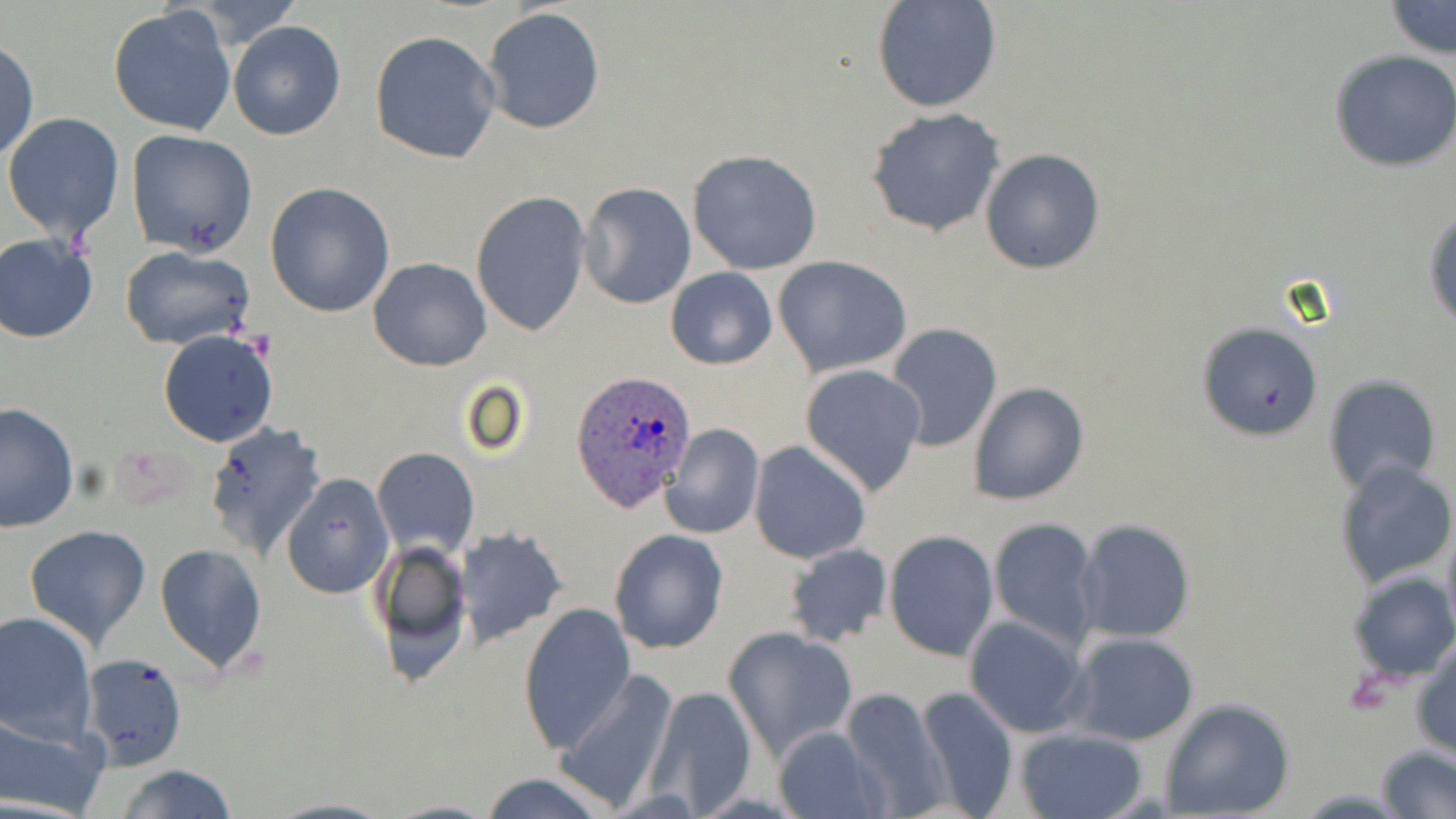 Approximate bounding boxes as [x1, y1, x2, y2] in pixels. Uninfected red blood cell locations: [192, 0, 300, 47], [871, 0, 1001, 114], [1385, 2, 1454, 59], [108, 5, 237, 135], [480, 7, 606, 136], [226, 21, 346, 141], [369, 31, 502, 164], [1, 39, 38, 165], [1328, 49, 1456, 172], [865, 108, 1005, 239], [3, 111, 125, 245], [126, 129, 258, 258], [979, 148, 1106, 275], [686, 150, 824, 275], [264, 182, 395, 319], [579, 182, 697, 310], [470, 190, 592, 338], [1425, 211, 1456, 335], [0, 234, 100, 342], [120, 246, 255, 350], [772, 255, 913, 378], [368, 257, 492, 370], [665, 267, 779, 369], [1199, 321, 1322, 440], [884, 322, 1003, 451], [157, 329, 277, 447], [800, 364, 927, 495], [1322, 375, 1442, 492], [968, 382, 1088, 505], [0, 401, 78, 533], [204, 422, 327, 560], [659, 422, 765, 539], [749, 441, 872, 565], [371, 447, 480, 559], [1333, 458, 1455, 592], [280, 473, 394, 597], [1441, 515, 1456, 644], [986, 516, 1101, 649], [1076, 518, 1197, 644], [24, 525, 152, 649], [455, 526, 569, 647], [607, 528, 729, 654], [884, 530, 998, 660], [373, 536, 472, 673], [783, 543, 892, 647], [154, 544, 269, 671], [1347, 568, 1456, 684], [518, 601, 634, 754], [0, 611, 98, 743], [963, 615, 1091, 739], [724, 626, 859, 759], [1066, 631, 1200, 746], [1410, 638, 1456, 760], [79, 653, 188, 768], [551, 670, 678, 812], [646, 685, 756, 815], [911, 685, 1019, 818], [839, 689, 953, 816], [1159, 698, 1296, 819], [0, 711, 110, 818], [772, 727, 888, 819], [1014, 727, 1148, 819], [1376, 745, 1456, 818], [117, 764, 236, 819], [478, 773, 610, 819], [267, 797, 395, 819], [383, 800, 502, 818]. Plasmodium ovale-infected red blood cell locations: [571, 371, 699, 511]. Slide-level diagnosis: Plasmodium ovale. May-Grünwald-Giemsa-stained preparation. Thin blood film. Captured at 1000x magnification. Image is 1456×819 pixels. One field of a larger specimen. Optical microscopy.